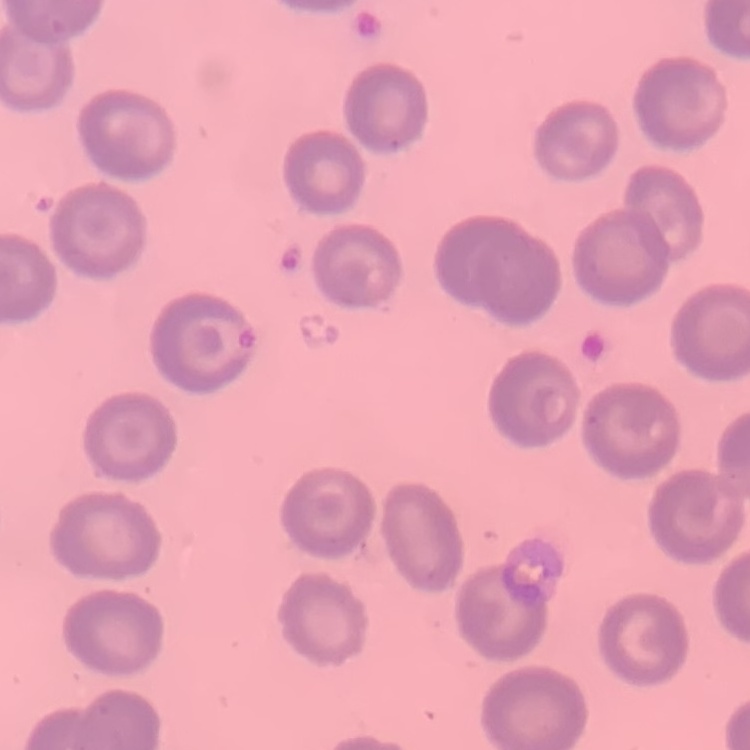

{
  "red_blood_cell_morphology": "no rouleaux formation",
  "image_type": "square crop of a larger photomicrograph",
  "stain": "Field's or Giemsa",
  "preparation": "thin blood film"
}